Classify this cell by malaria status.
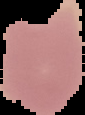
Uninfected.

From a thin blood smear. The area outside the segmented cell region is set to black. Image is 85×115 pixels.